Assess this cell for malaria.
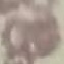

It is uninfected.

Summary:
  - Preparation: thin blood smear
  - Capture: smartphone through the microscope eyepiece
  - Stain: Giemsa
  - Image type: cell patch, automatically extracted from a larger field of view and resized to 64 × 64 pixels